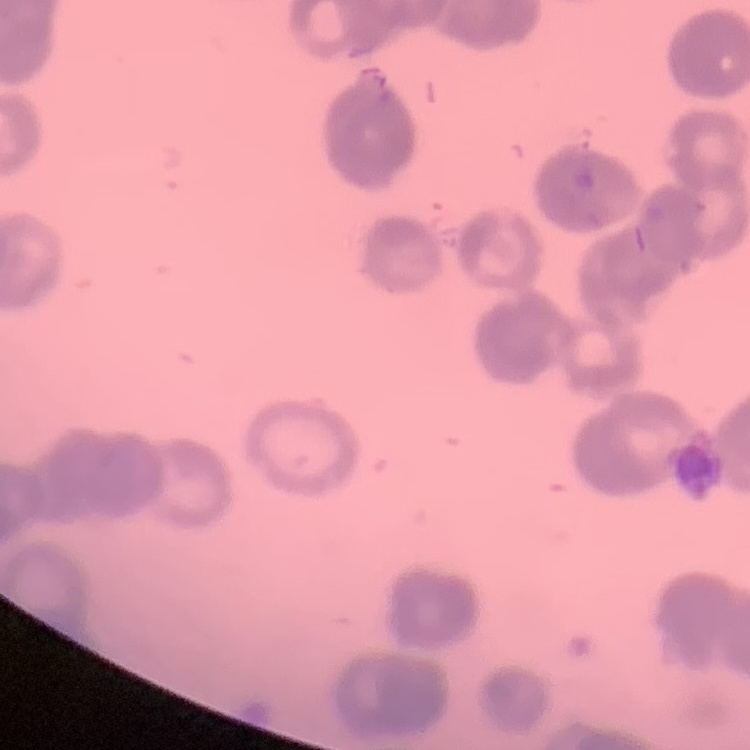

{
  "red_blood_cell_morphology": "rouleaux formation",
  "preparation": "thin peripheral smear",
  "stain": "Field's or Giemsa",
  "image_type": "square crop of a larger photomicrograph"
}